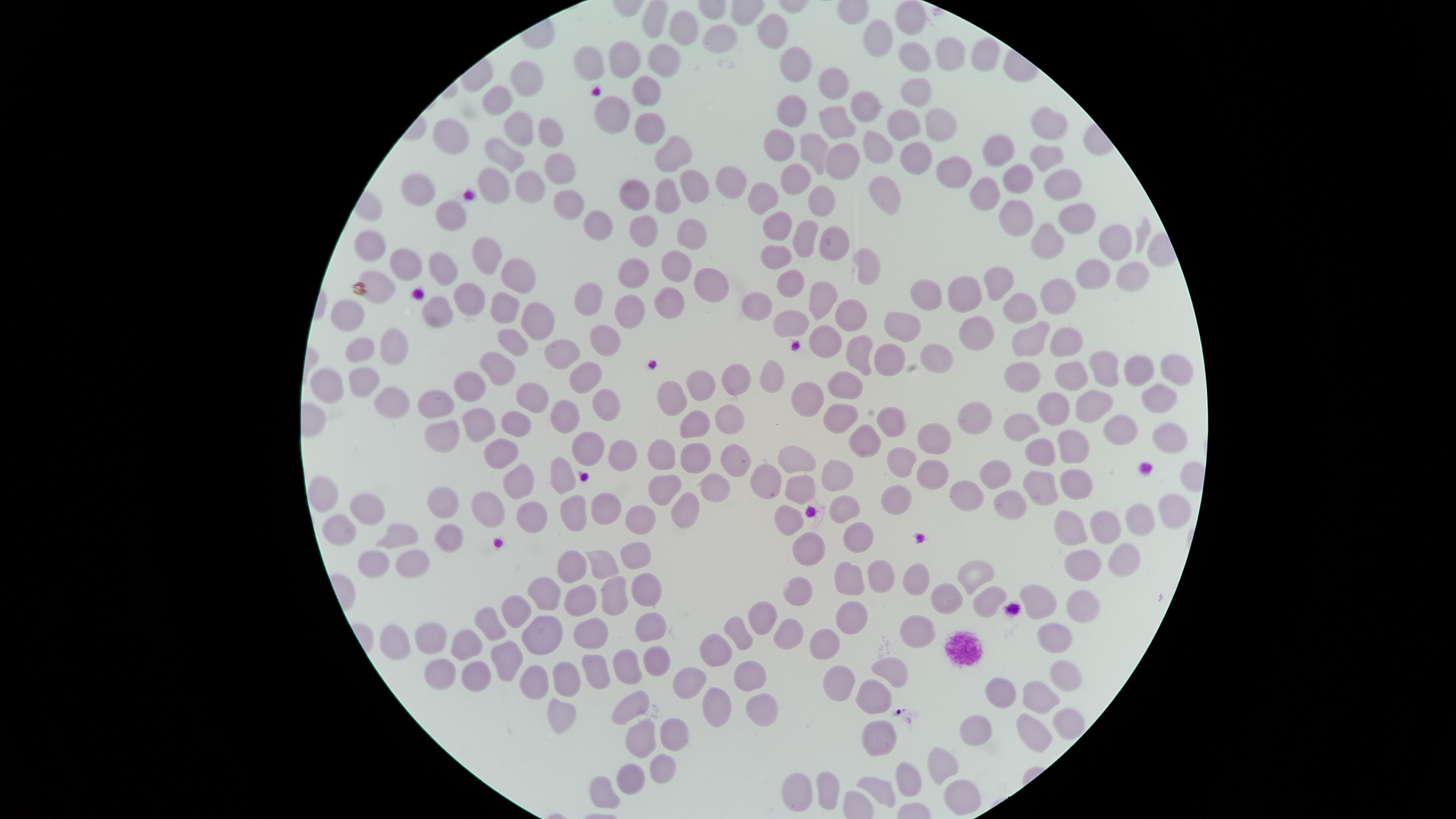

Approximate marker points as (x, y) in pixels.
Summary:
  - Uninfected red blood cells: (903, 19), (680, 25), (770, 27), (717, 39), (876, 42), (979, 53), (946, 55), (918, 58), (624, 63), (663, 63), (793, 64), (586, 68), (521, 84), (649, 88), (832, 89), (914, 91), (496, 99), (791, 111), (860, 113), (609, 119), (929, 120), (1045, 123), (518, 125), (833, 126), (898, 126), (647, 127), (552, 137), (453, 142), (780, 142), (988, 149), (817, 151), (877, 151), (504, 154), (671, 154), (913, 154), (1045, 161), (840, 163), (555, 165), (946, 172), (793, 178), (1018, 180), (1071, 180), (492, 186), (633, 186), (730, 186), (523, 187), (695, 188), (417, 189), (663, 195), (988, 195), (881, 198), (563, 199), (760, 200), (823, 201), (446, 213), (1016, 214), (593, 218), (1071, 222), (640, 225), (779, 228), (690, 236), (805, 236), (1044, 241), (1105, 242), (837, 247), (371, 249), (488, 257), (772, 263), (409, 264), (675, 270), (866, 270), (441, 271), (517, 271), (635, 272), (1124, 272), (1084, 279), (991, 285), (705, 287), (787, 287), (374, 290), (923, 296), (959, 297), (1057, 298), (473, 300), (823, 300), (593, 301), (664, 303), (629, 304), (754, 307), (434, 310), (1021, 310), (501, 311), (347, 312), (847, 313), (791, 323), (532, 324), (895, 326), (978, 332), (1026, 335), (601, 339), (826, 341), (1063, 341), (507, 344), (389, 346), (362, 347), (560, 349), (861, 356), (938, 357), (890, 358), (1130, 367), (1097, 369), (1168, 370), (1023, 372), (581, 373), (774, 373), (491, 375), (1065, 375), (735, 377), (330, 383), (468, 384), (361, 385), (698, 388), (851, 389), (669, 393), (810, 397), (392, 402), (440, 402), (1159, 402), (526, 403), (606, 404), (1100, 405), (1053, 409), (838, 412), (722, 413), (972, 413), (569, 417), (477, 419), (896, 420), (1022, 424), (511, 427), (693, 429), (1121, 429), (863, 439), (932, 439), (439, 441), (1165, 442), (590, 447), (1072, 447), (1036, 449), (498, 452), (623, 453), (660, 456), (733, 456), (694, 457), (907, 461), (793, 463), (994, 470), (561, 474), (931, 475), (837, 477), (515, 479), (768, 479), (1035, 483), (1072, 484), (713, 485), (326, 491), (798, 491), (665, 492), (961, 494), (892, 495), (443, 502), (1008, 506), (363, 508), (572, 509), (841, 509), (485, 510), (602, 510), (681, 513), (1174, 513), (531, 516), (639, 517), (1140, 518), (782, 525), (1077, 526), (335, 527), (1107, 527), (448, 533), (855, 535), (401, 538), (809, 553), (602, 555), (1122, 555), (635, 558), (410, 563), (569, 563), (373, 564), (1085, 570), (972, 577), (846, 578), (907, 579), (875, 580), (643, 590), (546, 596), (792, 596), (612, 599), (942, 599), (985, 599), (1036, 601), (578, 603), (1079, 609), (764, 614), (517, 616), (852, 616), (913, 626), (489, 627), (648, 632), (1053, 632), (540, 636), (586, 636), (393, 637), (432, 637), (735, 637), (792, 638), (469, 642), (822, 647), (714, 651), (507, 652), (654, 653), (623, 657), (590, 665), (442, 670), (890, 670), (474, 672), (561, 680), (693, 680), (746, 681), (1061, 682), (842, 687), (1001, 694), (871, 697), (1037, 698), (638, 703), (715, 706), (555, 710), (759, 711), (1066, 726), (1030, 730), (637, 731), (977, 731), (669, 732), (877, 739), (662, 765), (943, 766), (628, 772), (910, 782), (604, 787), (803, 787), (826, 790), (880, 791), (954, 794)
  - Preparation: thin blood smear
  - Presence: no malaria parasites identified
  - Stain: Giemsa
  - Field of view: single
  - Capture: smartphone photograph through the microscope eyepiece
  - Image size: 1456×819 pixels
  - Visible region: circular